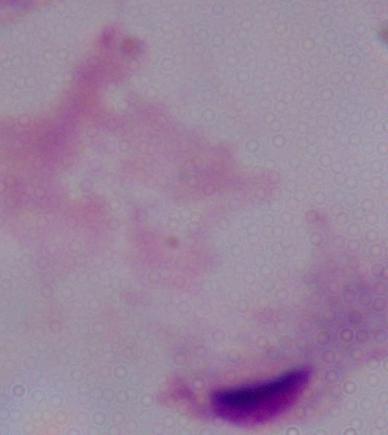
{
  "magnification": "1000x",
  "modality": "photomicrograph",
  "identification": "trichomonad"
}